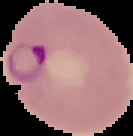
Image is 133×136 pixels. Cell region segmented out of the field of view; the surrounding area is masked to black. From a thin blood smear. Result: malaria parasites detected.